Identify the preparation type.
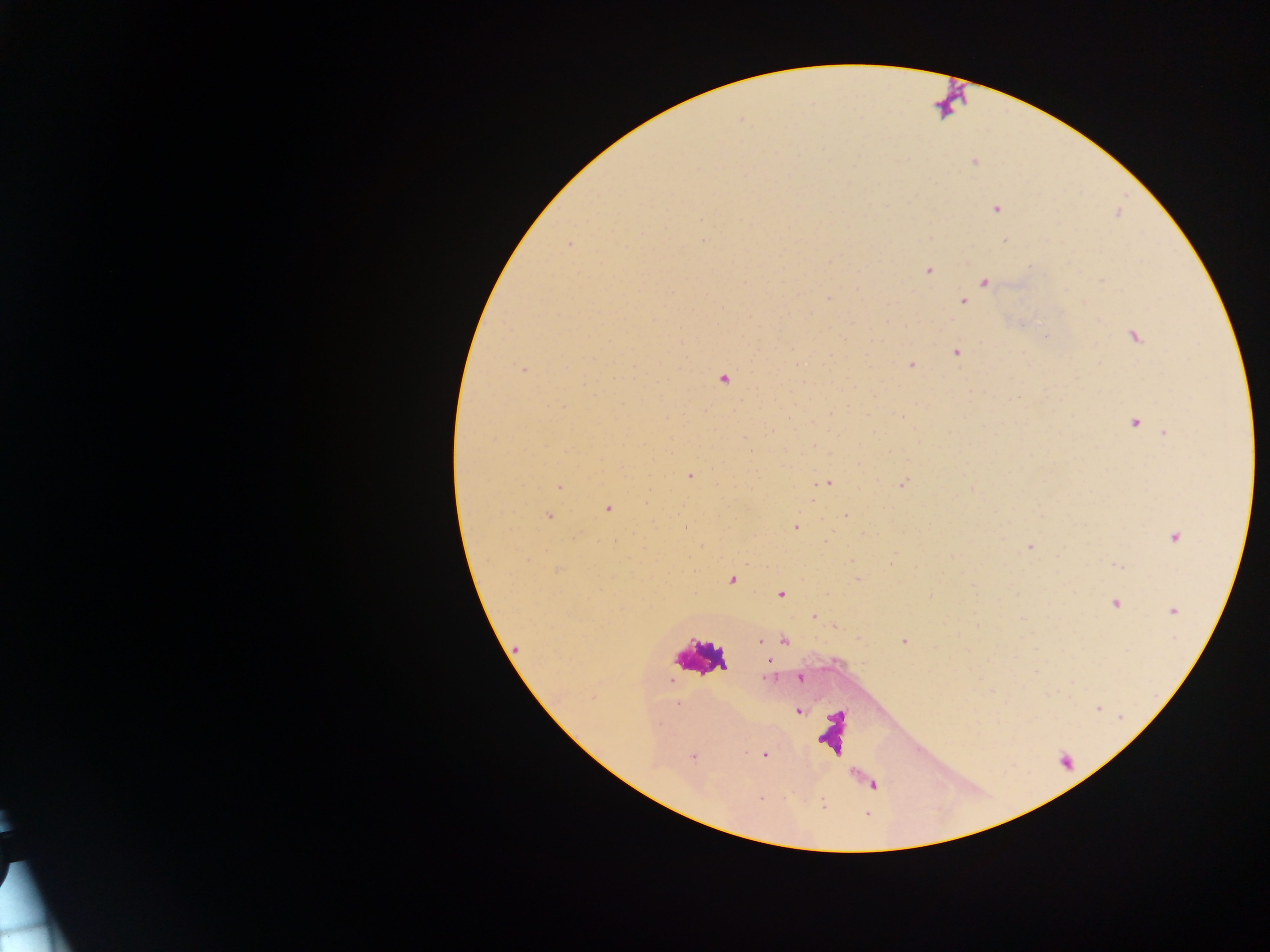

This is a thick smear.

Approximate centers as [x, y] in pixels.
Summary:
  - Malaria parasite locations: [972, 163], [994, 210], [701, 218], [703, 241], [1005, 241], [568, 245], [830, 261], [1031, 267], [928, 271], [984, 281], [1100, 281], [829, 297], [963, 301], [1083, 303], [722, 308], [1134, 334], [845, 336], [956, 353], [911, 364], [525, 370], [724, 378], [899, 417], [1134, 420], [769, 430], [744, 438], [814, 446], [690, 476], [829, 482], [899, 483], [823, 485], [560, 487], [607, 508], [846, 515], [549, 516], [796, 527], [1173, 537], [1027, 547], [1058, 556], [1118, 566], [857, 578], [732, 579], [782, 594], [930, 595], [1115, 605], [1171, 611], [813, 616], [835, 628], [860, 639], [758, 642], [904, 642], [514, 646], [768, 663], [799, 677], [768, 678], [677, 703], [798, 710], [659, 724], [765, 754], [692, 756], [759, 799]
  - Country: Ghana
  - Image size: 1270×952 pixels
  - Capture: mobile-phone photograph through a microscope
  - Field of view: single